Find each parasitized red blood cell.
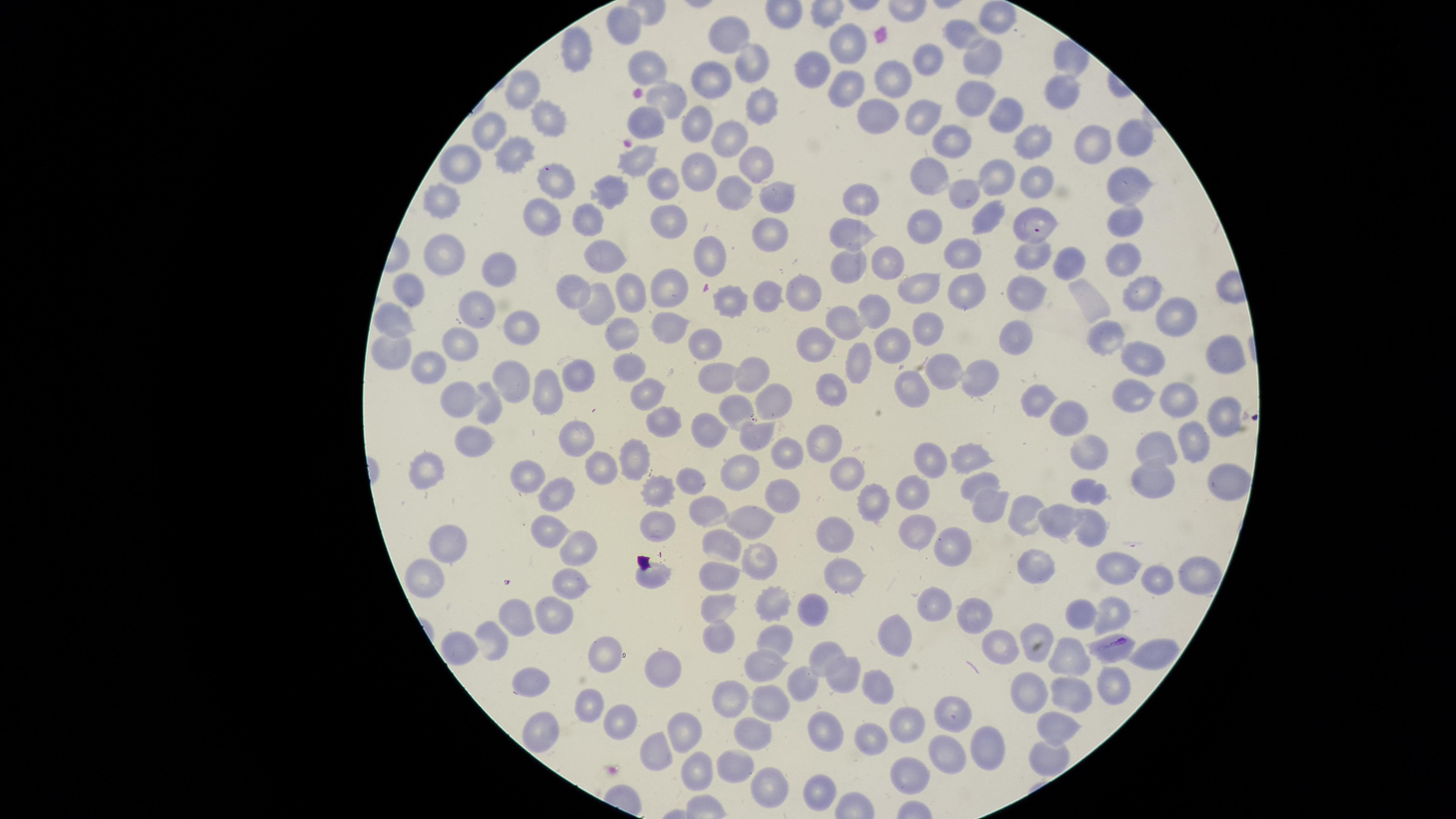

Approximate marker points as (x, y) in pixels.
Parasitized red blood cells: (1115, 647).

visible region = circular
field of view = single
capture = smartphone photograph through the microscope eyepiece
uninfected red blood cells = approximate marker points as (x, y) in pixels: (998, 21), (622, 26), (733, 35), (960, 35), (849, 43), (583, 45), (927, 57), (1069, 57), (982, 60), (754, 63), (653, 64), (820, 67), (895, 74), (714, 78), (524, 87), (839, 90), (975, 93), (1063, 94), (666, 95), (758, 99), (875, 112), (920, 113), (542, 117), (1006, 117), (698, 119), (647, 121), (493, 132), (727, 137), (949, 140), (1036, 140), (1130, 140), (1094, 141), (518, 146), (636, 159), (758, 159), (463, 160), (703, 164), (933, 174), (996, 179), (1037, 179), (559, 180), (668, 182), (1126, 186), (965, 188), (611, 191), (732, 191), (774, 195), (867, 196), (446, 198), (548, 211), (1038, 214), (988, 218), (589, 219), (669, 219), (1126, 222), (929, 223), (854, 230), (769, 232), (447, 248), (714, 252), (600, 253), (966, 253), (1036, 257), (1060, 260), (1120, 260), (891, 261), (849, 264), (505, 267), (668, 280), (914, 283), (579, 286), (967, 287), (1028, 289), (412, 290), (1139, 290), (637, 291), (807, 291), (768, 294), (733, 298), (603, 303), (476, 305), (880, 311), (1171, 315), (847, 318), (398, 320), (524, 320), (929, 323), (670, 324), (624, 331), (1019, 331), (1110, 332), (708, 341), (821, 342), (463, 343), (893, 346), (388, 350), (863, 356), (1214, 356), (1145, 359), (427, 367), (636, 367), (952, 367), (755, 372), (582, 373), (719, 373), (987, 373), (516, 378), (915, 378), (828, 386), (550, 389), (1173, 394), (1132, 395), (650, 396), (773, 396), (1042, 396), (462, 397), (737, 404), (491, 406), (1216, 412), (1070, 414), (663, 421), (712, 421), (761, 428), (576, 434), (823, 439), (1195, 439), (472, 444), (1091, 444), (1161, 445), (791, 450), (632, 455), (971, 455), (600, 463), (932, 463), (426, 466), (845, 470), (743, 472), (1226, 480), (534, 481), (980, 481), (695, 483), (1150, 483), (559, 487), (659, 488), (912, 492), (1096, 492), (785, 493), (872, 496), (991, 502), (703, 507), (1054, 515), (1024, 516), (1090, 521), (755, 524), (656, 525), (547, 528), (911, 528), (839, 531), (722, 537), (456, 539), (952, 546), (576, 549), (1036, 558), (757, 559), (720, 570), (1112, 570), (1192, 575), (655, 576), (569, 578), (843, 579), (418, 582), (1154, 583), (719, 601), (779, 601), (935, 602), (815, 606), (558, 610), (520, 611), (972, 611), (1081, 612), (1112, 612), (776, 635), (899, 635), (493, 641), (1000, 642), (1040, 649), (460, 651), (605, 651), (825, 651), (1151, 651), (1064, 657), (763, 660), (664, 662), (844, 671), (534, 679), (1034, 680), (803, 685), (1113, 685), (880, 689), (1072, 692), (737, 693), (774, 699), (588, 702), (950, 709), (622, 713), (541, 723), (905, 727), (1056, 729), (823, 730), (688, 733), (755, 736), (872, 741), (988, 745), (652, 756), (1049, 757), (945, 758), (733, 766), (910, 773), (696, 774), (767, 788), (815, 792)
preparation = thin blood smear
stain = Giemsa
species = Plasmodium falciparum
image size = 1456×819 pixels